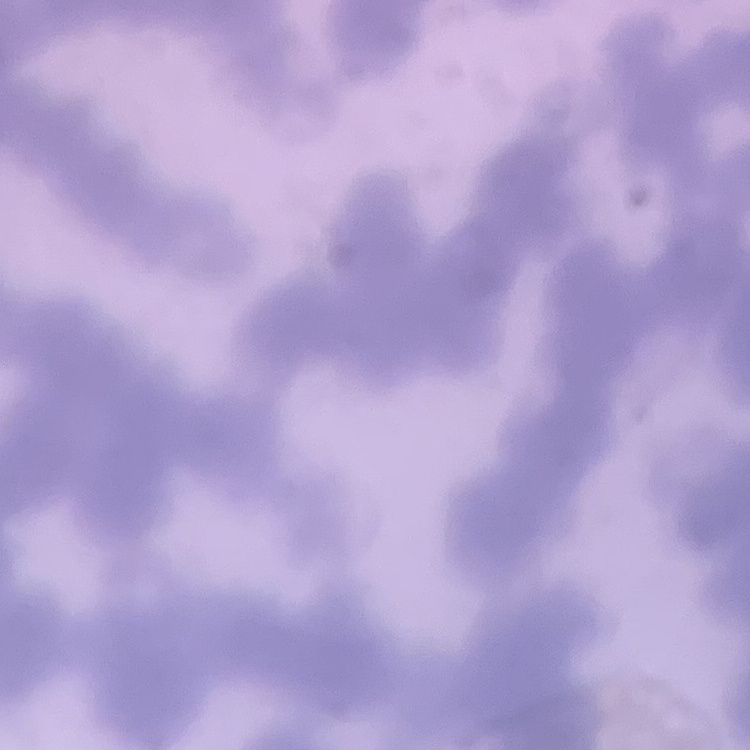

red blood cell morphology = rouleaux formation
preparation = thin blood smear
image type = one tile cut from a larger photomicrograph
stain = Field's or Giemsa